Outline each Plasmodium ovale-infected red blood cell.
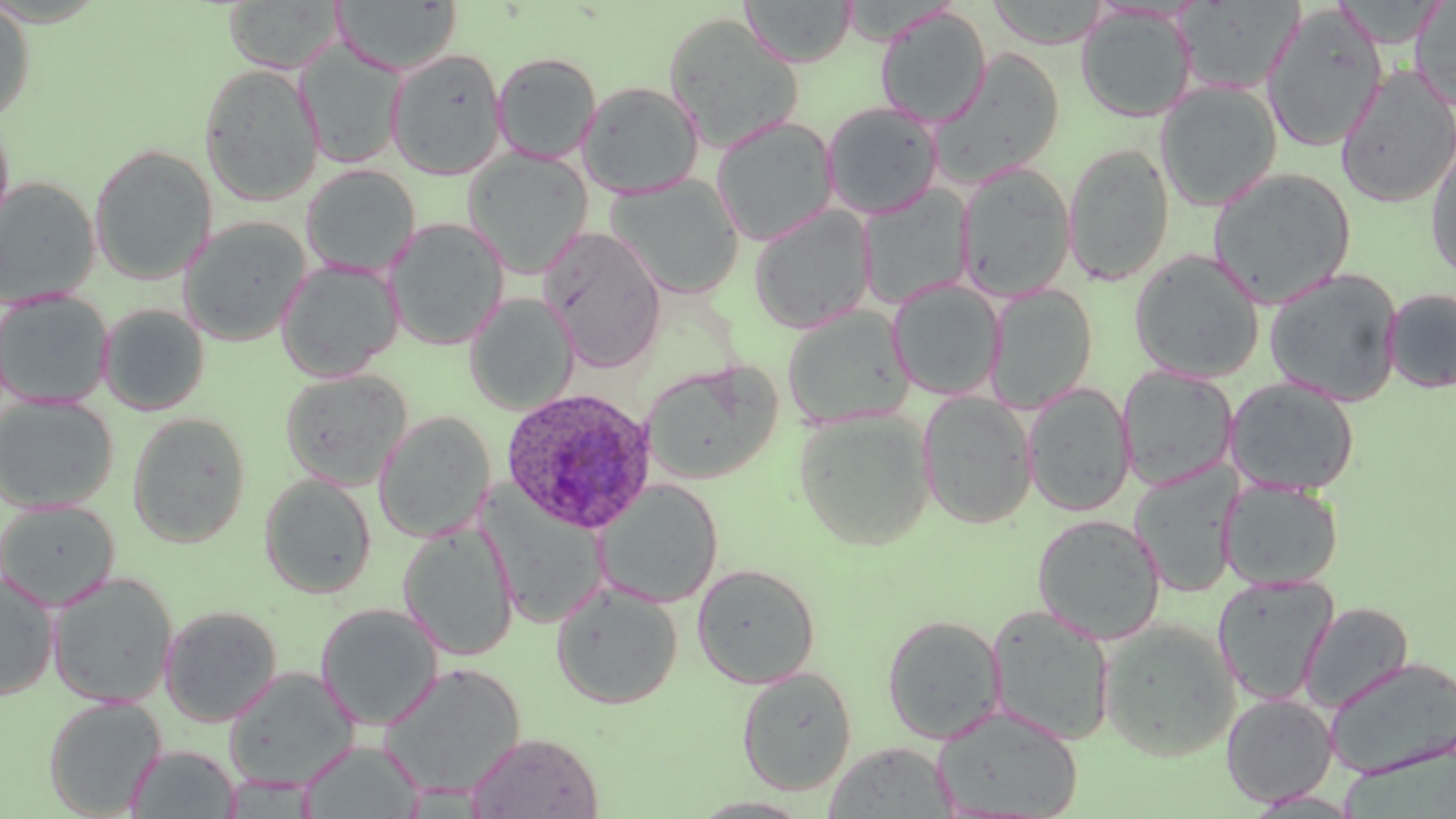
Approximate bounding boxes as named x1/y1/x2/y2 corners in pixels.
Plasmodium ovale-infected red blood cells: (x1=499, y1=386, x2=657, y2=534).

Uninfected red blood cell locations: (x1=740, y1=0, x2=857, y2=67), (x1=0, y1=1, x2=35, y2=124), (x1=223, y1=1, x2=343, y2=73), (x1=331, y1=1, x2=463, y2=75), (x1=985, y1=1, x2=1112, y2=49), (x1=1410, y1=1, x2=1456, y2=111), (x1=1261, y1=5, x2=1387, y2=153), (x1=874, y1=6, x2=992, y2=128), (x1=1076, y1=6, x2=1198, y2=123), (x1=661, y1=12, x2=804, y2=153), (x1=296, y1=40, x2=408, y2=170), (x1=385, y1=47, x2=507, y2=180), (x1=930, y1=48, x2=1065, y2=187), (x1=492, y1=52, x2=602, y2=164), (x1=198, y1=62, x2=325, y2=206), (x1=1335, y1=67, x2=1456, y2=208), (x1=577, y1=80, x2=704, y2=199), (x1=1155, y1=80, x2=1283, y2=212), (x1=821, y1=101, x2=944, y2=219), (x1=710, y1=116, x2=839, y2=246), (x1=1426, y1=139, x2=1456, y2=283), (x1=1062, y1=143, x2=1175, y2=286), (x1=88, y1=144, x2=217, y2=284), (x1=462, y1=148, x2=593, y2=278), (x1=956, y1=162, x2=1076, y2=301), (x1=301, y1=164, x2=420, y2=277), (x1=1207, y1=167, x2=1357, y2=308), (x1=607, y1=174, x2=745, y2=299), (x1=0, y1=177, x2=100, y2=306), (x1=858, y1=186, x2=974, y2=309), (x1=749, y1=205, x2=876, y2=334), (x1=178, y1=216, x2=311, y2=347), (x1=384, y1=217, x2=509, y2=351), (x1=539, y1=226, x2=666, y2=372), (x1=1129, y1=250, x2=1265, y2=383), (x1=276, y1=259, x2=403, y2=382), (x1=1263, y1=268, x2=1404, y2=407), (x1=887, y1=279, x2=1005, y2=401), (x1=986, y1=284, x2=1098, y2=413), (x1=1383, y1=288, x2=1456, y2=394), (x1=0, y1=290, x2=114, y2=409), (x1=465, y1=293, x2=580, y2=416), (x1=98, y1=303, x2=210, y2=416), (x1=782, y1=305, x2=915, y2=429), (x1=643, y1=361, x2=782, y2=486), (x1=1118, y1=365, x2=1239, y2=490), (x1=280, y1=368, x2=412, y2=491), (x1=1225, y1=377, x2=1361, y2=496), (x1=1023, y1=383, x2=1135, y2=516), (x1=917, y1=391, x2=1038, y2=529), (x1=0, y1=395, x2=118, y2=513), (x1=794, y1=409, x2=936, y2=551), (x1=374, y1=411, x2=495, y2=542), (x1=127, y1=412, x2=251, y2=547), (x1=1130, y1=463, x2=1242, y2=597), (x1=259, y1=473, x2=377, y2=599), (x1=593, y1=479, x2=725, y2=609), (x1=1220, y1=479, x2=1344, y2=590), (x1=483, y1=493, x2=609, y2=630), (x1=0, y1=500, x2=120, y2=612), (x1=1031, y1=513, x2=1166, y2=644), (x1=398, y1=522, x2=519, y2=662), (x1=692, y1=563, x2=821, y2=688), (x1=0, y1=571, x2=60, y2=701), (x1=46, y1=572, x2=178, y2=708), (x1=1213, y1=575, x2=1339, y2=705), (x1=551, y1=581, x2=683, y2=710), (x1=1299, y1=601, x2=1413, y2=712), (x1=314, y1=602, x2=443, y2=731), (x1=985, y1=604, x2=1116, y2=746), (x1=159, y1=605, x2=283, y2=726), (x1=881, y1=614, x2=1006, y2=743), (x1=1098, y1=620, x2=1240, y2=761), (x1=1324, y1=656, x2=1456, y2=779), (x1=376, y1=662, x2=528, y2=799), (x1=736, y1=665, x2=857, y2=796), (x1=223, y1=667, x2=361, y2=791), (x1=1221, y1=693, x2=1338, y2=806), (x1=42, y1=696, x2=167, y2=818), (x1=932, y1=705, x2=1083, y2=819), (x1=466, y1=732, x2=604, y2=818), (x1=299, y1=740, x2=424, y2=819), (x1=823, y1=741, x2=959, y2=818), (x1=126, y1=745, x2=241, y2=818), (x1=688, y1=795, x2=818, y2=817). Slide-level diagnosis: Plasmodium ovale. Light microscopy. Thin blood smear. May-Grünwald-Giemsa-stained preparation. Captured at 1000x magnification. Image is 1456×819 pixels. One field of a larger specimen.